Name the parasite shown.
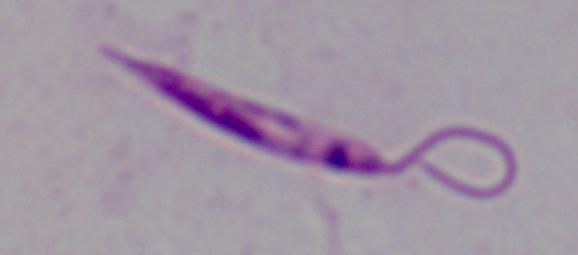
Leishmania.

{
  "magnification": "1000x",
  "modality": "photomicrograph"
}